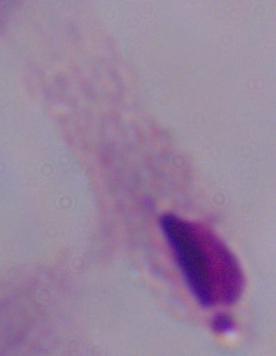
magnification = 1000x
identification = trichomonad
modality = micrograph